Assess this cell for malaria.
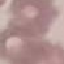
It is uninfected.

Photographed with a smartphone camera at the microscope eyepiece. Giemsa stain. Cell patch, automatically extracted from a larger field of view and resized to 64 × 64 pixels. Thin blood smear.